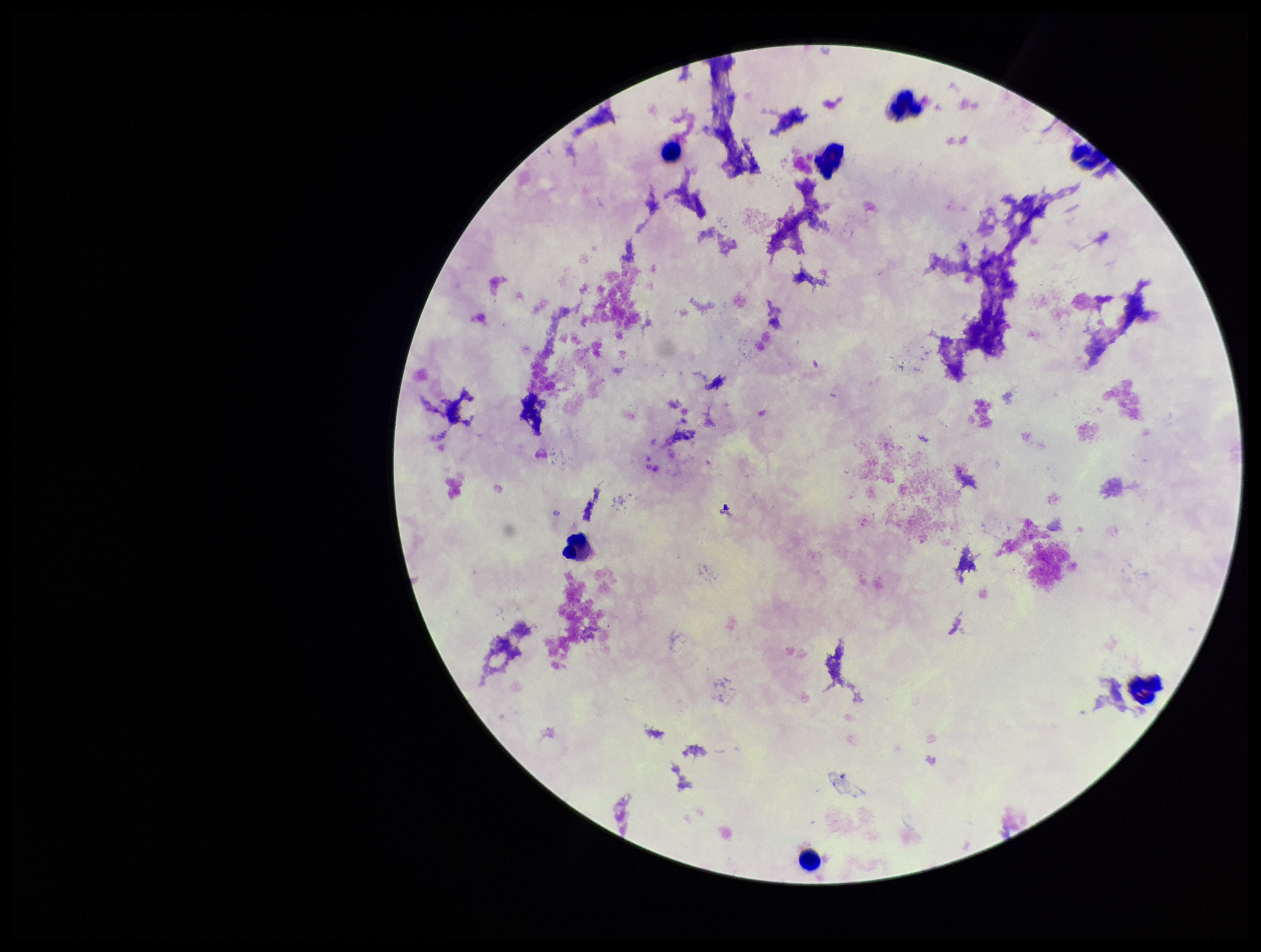

capture = smartphone photograph through the microscope eyepiece
patient malaria status = negative
leukocyte count = 7
field of view = one from this slide
parasite count = 0
preparation = thick blood smear
image size = 1261×952 pixels
stain = Giemsa
Plasmodium parasites = none seen